Assess this cell for malaria.
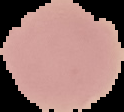

It is uninfected.

image size = 124×112 pixels
preparation = thin blood smear
image type = segmented cell region with the area outside set to black